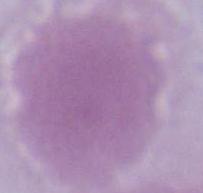 Captured at 1000x magnification. Micrograph. An erythrocyte is shown.